State which parasite is depicted.
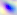
Toxoplasma gondii.

magnification = 400x
modality = micrograph